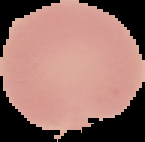

image size = 145×142 pixels
preparation = thin blood smear
image type = segmented cell region on a black background
result = negative for Plasmodium parasites